Assess for malaria.
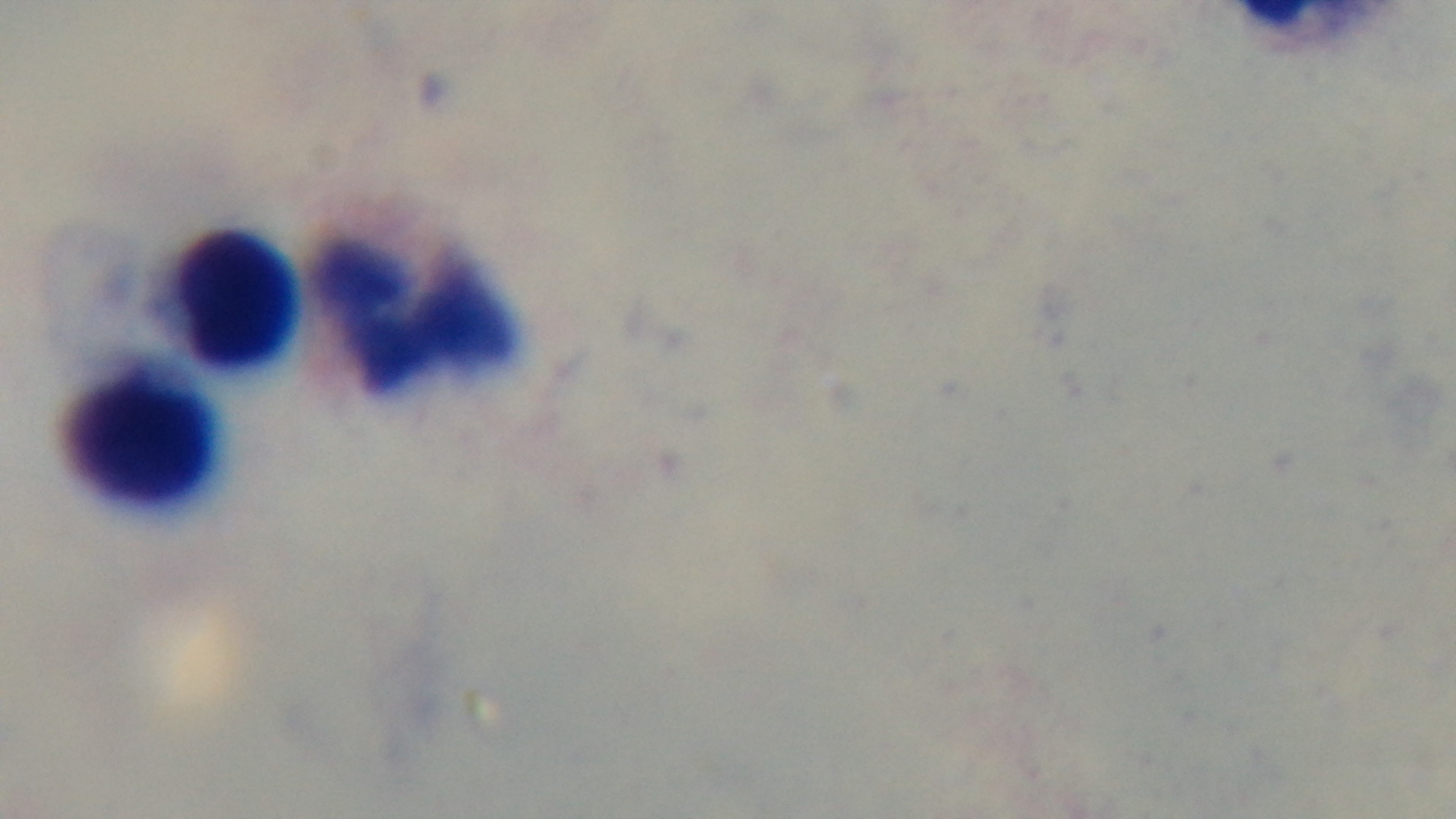

It is uninfected.

preparation = thick smear
stain = Giemsa
objective = 100x oil immersion
field of view = one from the slide
modality = light microscopy
capture = mounted 4K digital camera